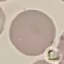

Malaria status: uninfected. Cell patch, automatically extracted from a larger field of view and resized to 64 × 64 pixels. Thin smear of blood. Giemsa stain. Acquired by smartphone through the microscope eyepiece.